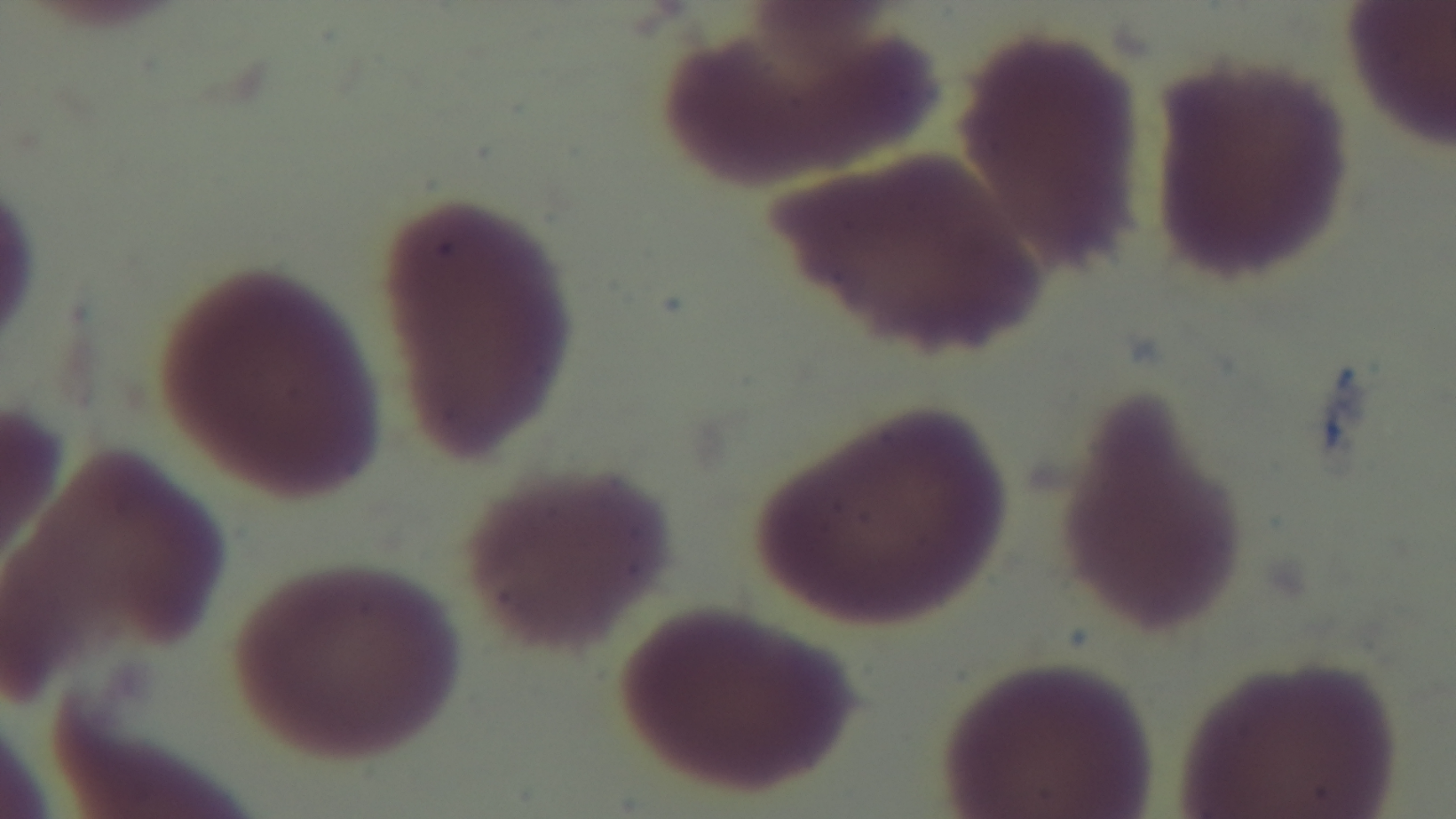
{
  "field_of_view": "one from the slide",
  "malaria_status": "negative",
  "preparation": "thin smear",
  "objective": "100x oil immersion",
  "modality": "light microscopy",
  "capture": "mounted 4K digital camera",
  "stain": "Giemsa"
}